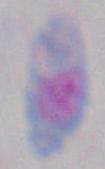 1000x magnification. Toxoplasma gondii is seen. Photomicrograph.